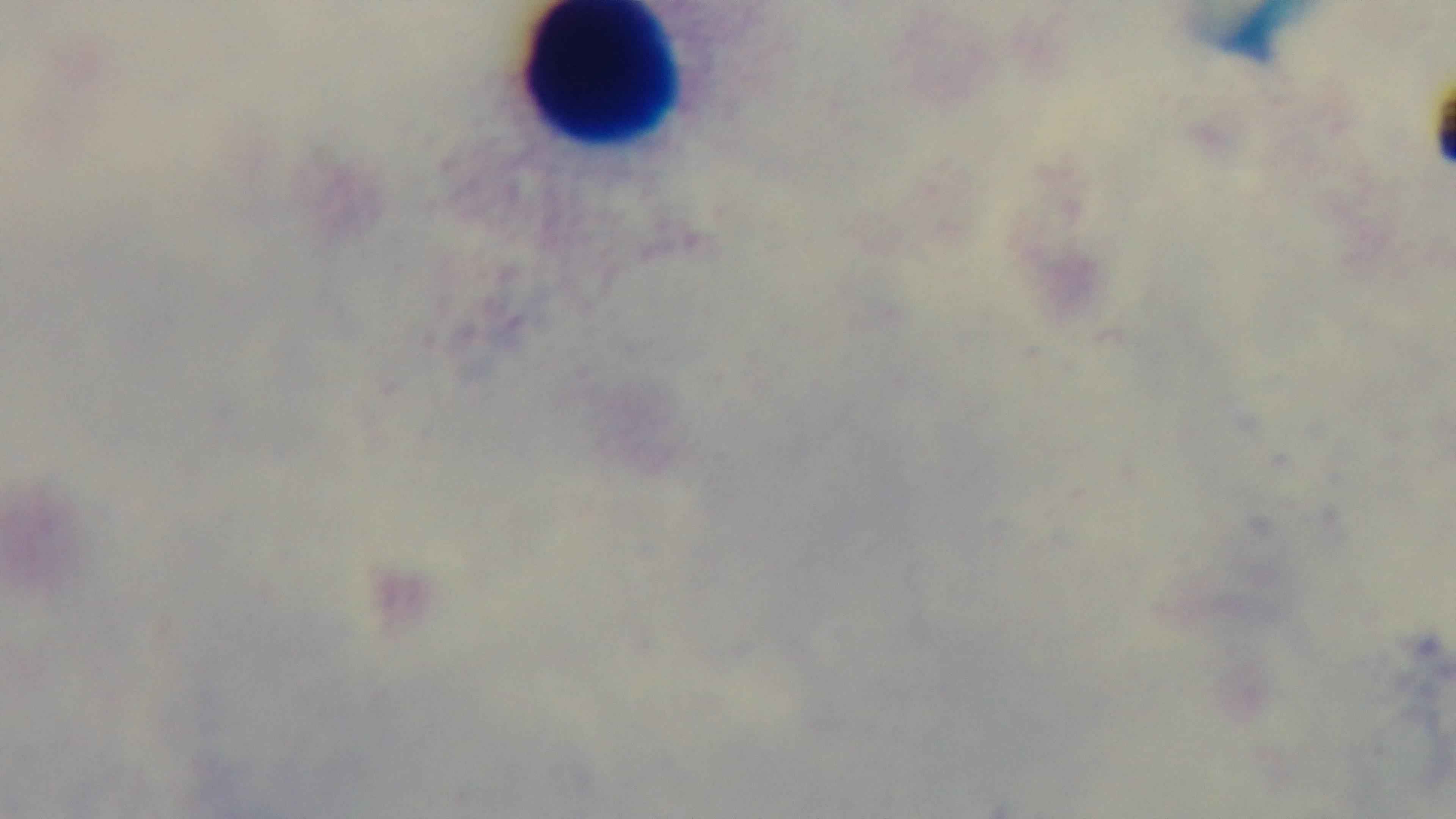

preparation = thick blood film
stain = Giemsa
modality = light microscopy
malaria status = uninfected
objective = 100x oil immersion
field of view = single
capture = mounted 4K digital camera